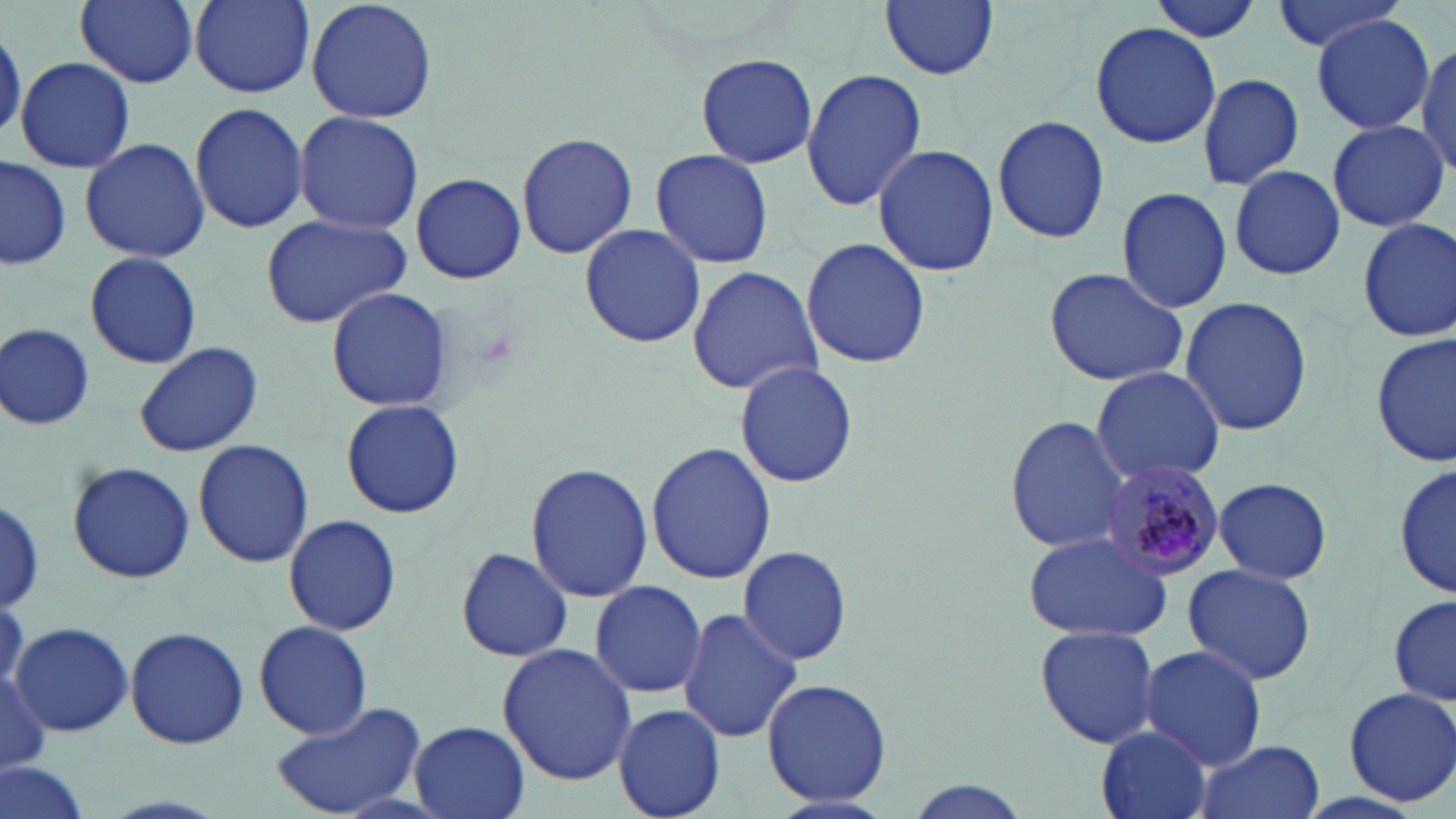

{
  "slide_level_diagnosis": "Plasmodium malariae",
  "field_of_view": "single",
  "stain": "May-Grünwald-Giemsa",
  "plasmodium_malariae_infected_red_blood_cell_locations": "approximate bounding boxes as (x1,y1)-(x2,y2) corner pairs in pixels: (1094,460)-(1226,579)",
  "preparation": "thin blood smear",
  "modality": "optical microscopy",
  "image_size": "1456×819 pixels",
  "uninfected_red_blood_cell_locations": "approximate bounding boxes as (x1,y1)-(x2,y2) corner pairs in pixels: (75,0)-(198,88), (186,0)-(318,100), (306,0)-(438,123), (880,0)-(1000,80), (1148,0)-(1267,43), (1270,0)-(1408,55), (1312,15)-(1435,133), (1090,20)-(1220,150), (1,26)-(25,143), (1414,39)-(1455,178), (695,54)-(817,169), (15,58)-(135,173), (801,67)-(926,212), (1195,70)-(1306,191), (190,100)-(307,233), (294,110)-(423,234), (992,113)-(1109,245), (1326,119)-(1449,232), (516,131)-(638,259), (79,137)-(211,262), (874,142)-(996,278), (650,148)-(774,269), (0,156)-(71,270), (1227,164)-(1345,280), (410,172)-(525,283), (1116,186)-(1233,314), (260,215)-(411,328), (1355,216)-(1455,345), (578,224)-(706,350), (801,236)-(930,370), (84,250)-(202,370), (686,264)-(821,395), (1043,267)-(1189,386), (325,285)-(454,413), (1179,297)-(1314,436), (2,324)-(96,430), (1372,331)-(1454,469), (133,342)-(262,459), (731,358)-(861,488), (1090,366)-(1226,485), (340,398)-(464,519), (1005,418)-(1131,553), (194,439)-(314,568), (645,442)-(775,585), (1393,456)-(1455,603), (525,462)-(654,602), (68,463)-(194,582), (1214,475)-(1332,584), (1,498)-(45,610), (284,514)-(402,636), (1022,531)-(1173,642), (455,544)-(574,664), (737,546)-(853,668), (1180,562)-(1318,685), (587,579)-(707,700), (1389,595)-(1455,707), (677,606)-(804,744), (11,620)-(134,736), (254,620)-(372,740), (1034,625)-(1161,749), (126,627)-(249,750), (497,643)-(636,786), (1138,644)-(1269,770), (0,666)-(51,777), (759,676)-(892,807), (1343,686)-(1456,806), (270,700)-(428,817), (614,703)-(727,818), (405,723)-(531,819), (1095,726)-(1213,819), (1194,739)-(1325,819), (1,760)-(91,819), (895,778)-(1037,819)",
  "magnification": "1000x"
}